Name the parasite shown.
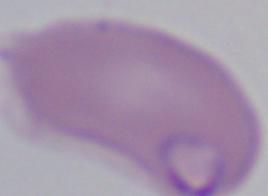

Babesia.

Summary:
  - Magnification: 1000x
  - Modality: photomicrograph